Classify this cell by malaria status.
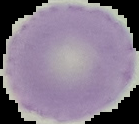

It is uninfected.

Segmented cell region on a black background. Image is 139×124 pixels. From a thin blood film.